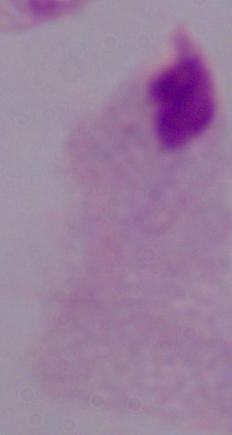
{
  "magnification": "1000x",
  "identification": "trichomonad",
  "modality": "photomicrograph"
}